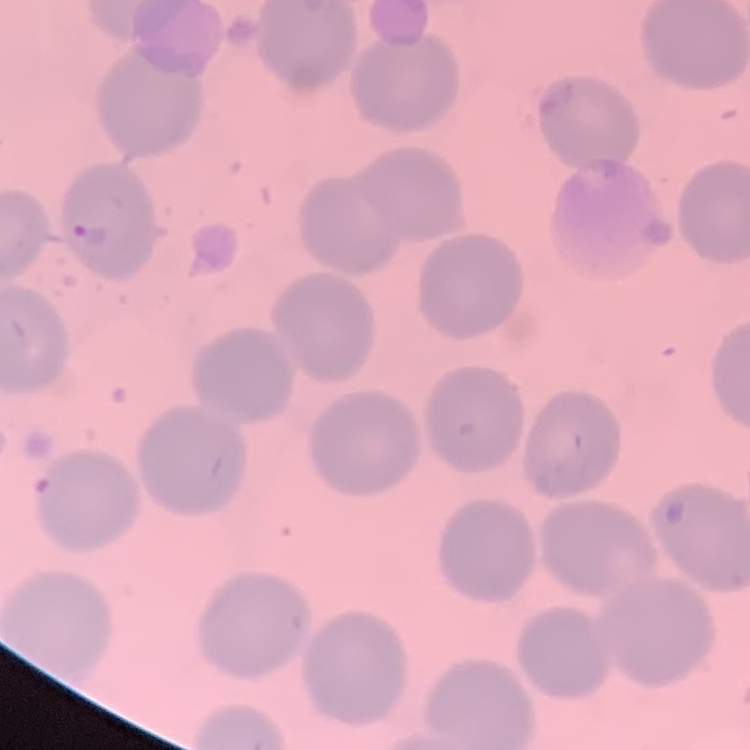

Summary:
  - Red blood cell morphology: no rouleaux formation
  - Stain: Field's or Giemsa
  - Preparation: thin peripheral smear
  - Image type: square crop of a larger photomicrograph